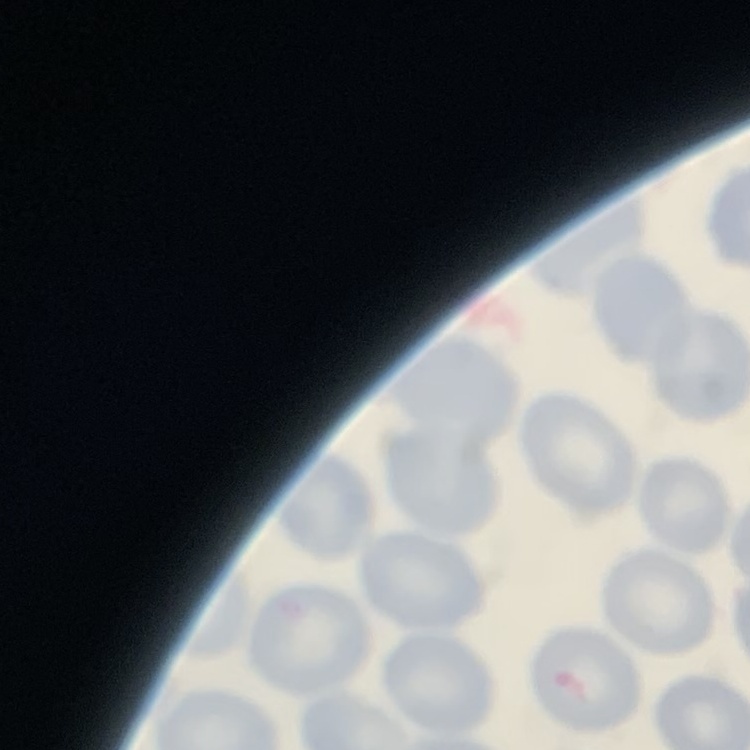
red blood cell morphology = no rouleaux formation
stain = Field's or Giemsa
image type = one tile cut from a larger photomicrograph
preparation = thin blood film